Comment on the morphology of the erythrocytes.
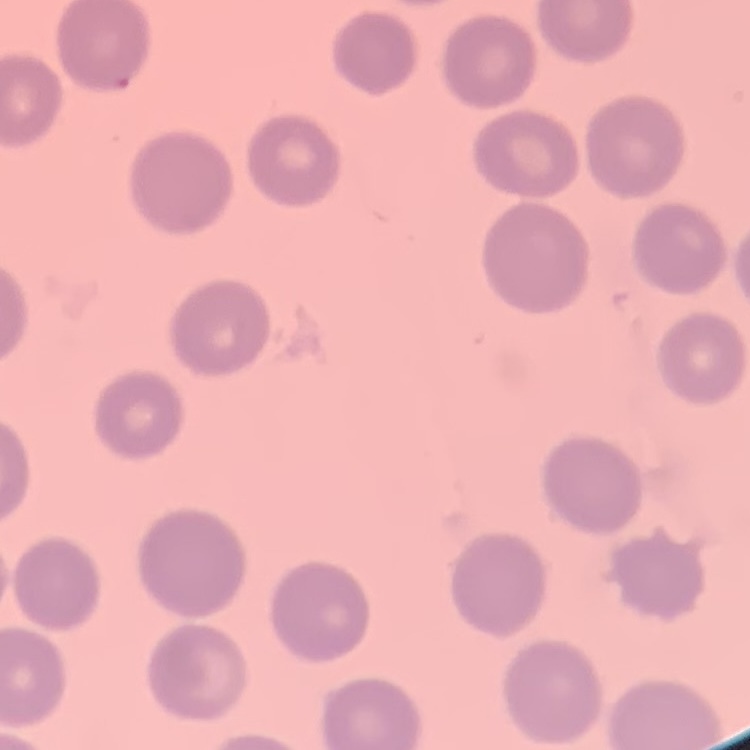

They show no rouleaux formation.

preparation = thin blood film
image type = square crop of a larger photomicrograph
stain = Field's or Giemsa